Identify the parasite.
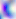

This is Toxoplasma gondii.

Summary:
  - Modality: micrograph
  - Magnification: 400x